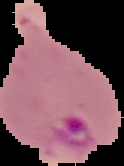

image type = cell region segmented out of the field of view; surrounding area masked to black
image size = 124×166 pixels
malaria status = parasitized
preparation = thin blood smear